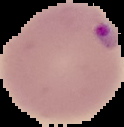
preparation = thin blood smear
image type = segmented cell region on a black background
malaria status = parasitized
image size = 124×127 pixels